Report the malaria status of this cell.
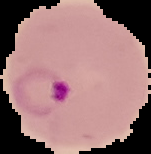
It is parasitized.

Summary:
  - Preparation: thin blood smear
  - Image type: cell region segmented out of the field of view; surrounding area masked to black
  - Image size: 151×154 pixels